Classify this cell by malaria status.
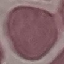
Uninfected.

Photographed with a smartphone camera at the microscope eyepiece. Giemsa-stained preparation. Thin blood smear. Cell patch, automatically extracted from a larger field of view and resized to 64 × 64 pixels.